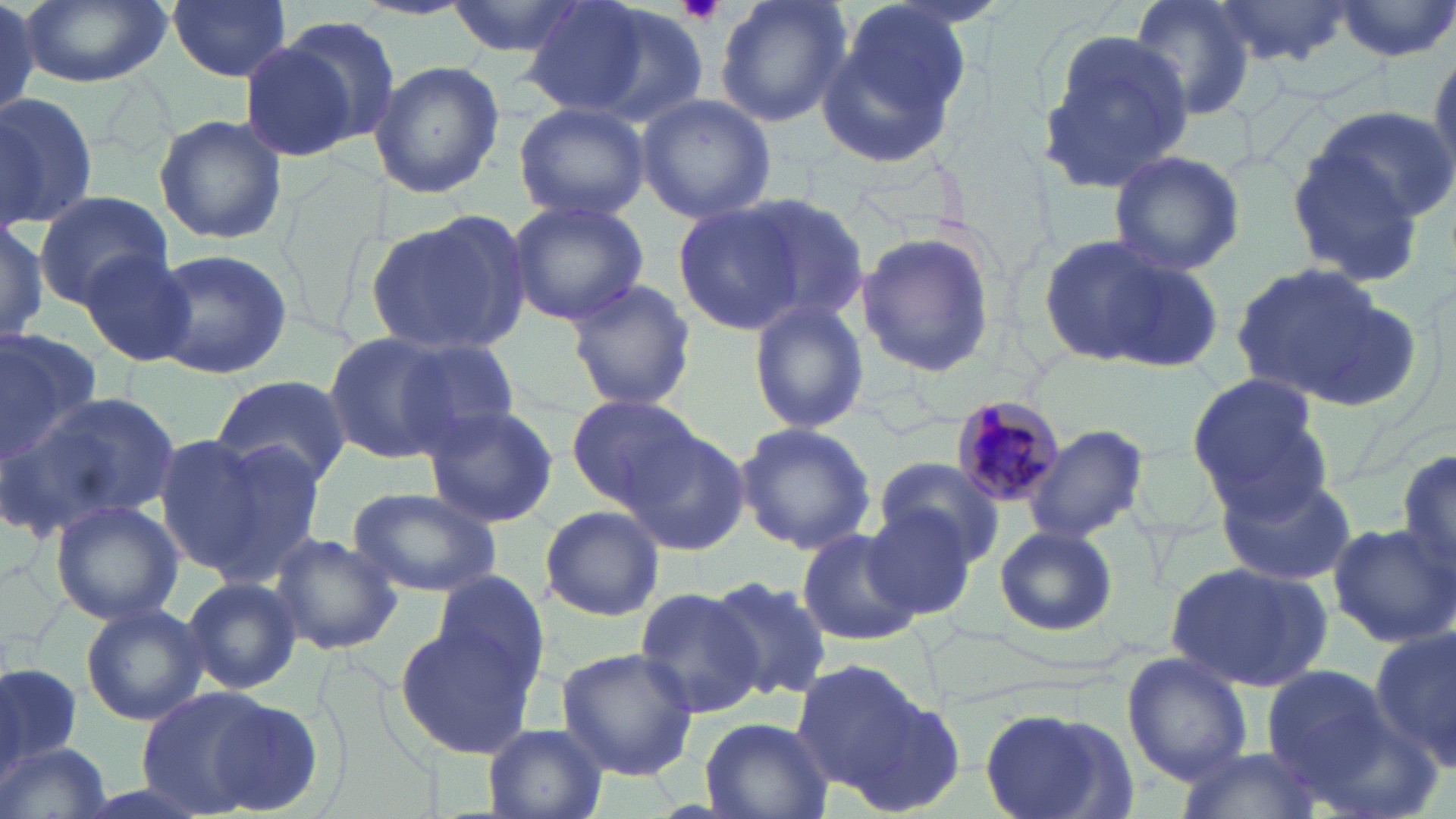

slide-level diagnosis = Plasmodium malariae
uninfected red blood cell locations = approximate bounding boxes as named x1/y1/x2/y2 corners in pixels: (x1=20, y1=0, x2=172, y2=88), (x1=165, y1=0, x2=293, y2=82), (x1=442, y1=0, x2=592, y2=59), (x1=523, y1=0, x2=684, y2=122), (x1=715, y1=0, x2=851, y2=128), (x1=1128, y1=0, x2=1258, y2=124), (x1=1216, y1=0, x2=1356, y2=69), (x1=0, y1=1, x2=50, y2=121), (x1=1333, y1=1, x2=1456, y2=61), (x1=817, y1=7, x2=971, y2=170), (x1=275, y1=15, x2=403, y2=148), (x1=1037, y1=29, x2=1197, y2=197), (x1=240, y1=42, x2=363, y2=161), (x1=1427, y1=43, x2=1456, y2=189), (x1=369, y1=60, x2=504, y2=197), (x1=0, y1=89, x2=101, y2=227), (x1=635, y1=93, x2=776, y2=224), (x1=514, y1=102, x2=651, y2=223), (x1=1307, y1=104, x2=1453, y2=224), (x1=154, y1=114, x2=289, y2=247), (x1=1284, y1=145, x2=1431, y2=288), (x1=1104, y1=150, x2=1246, y2=278), (x1=33, y1=189, x2=172, y2=307), (x1=739, y1=194, x2=869, y2=324), (x1=506, y1=198, x2=649, y2=326), (x1=674, y1=203, x2=807, y2=333), (x1=365, y1=210, x2=530, y2=356), (x1=0, y1=211, x2=52, y2=348), (x1=855, y1=229, x2=995, y2=380), (x1=1034, y1=231, x2=1195, y2=366), (x1=147, y1=246, x2=293, y2=381), (x1=75, y1=249, x2=197, y2=367), (x1=1098, y1=253, x2=1225, y2=376), (x1=1225, y1=260, x2=1416, y2=408), (x1=561, y1=278, x2=697, y2=413), (x1=747, y1=299, x2=871, y2=434), (x1=0, y1=326, x2=103, y2=460), (x1=320, y1=333, x2=467, y2=465), (x1=385, y1=333, x2=523, y2=453), (x1=1186, y1=371, x2=1329, y2=511), (x1=210, y1=373, x2=351, y2=491), (x1=13, y1=389, x2=182, y2=537), (x1=564, y1=394, x2=705, y2=506), (x1=420, y1=403, x2=559, y2=529), (x1=735, y1=421, x2=878, y2=554), (x1=620, y1=425, x2=750, y2=556), (x1=1023, y1=425, x2=1147, y2=545), (x1=152, y1=436, x2=273, y2=575), (x1=197, y1=436, x2=333, y2=581), (x1=1396, y1=447, x2=1456, y2=580), (x1=874, y1=457, x2=1004, y2=566), (x1=1212, y1=470, x2=1356, y2=586), (x1=346, y1=484, x2=504, y2=597), (x1=49, y1=499, x2=186, y2=626), (x1=863, y1=503, x2=981, y2=622), (x1=539, y1=504, x2=665, y2=621), (x1=1326, y1=520, x2=1454, y2=647), (x1=994, y1=524, x2=1118, y2=638), (x1=796, y1=527, x2=921, y2=647), (x1=267, y1=531, x2=404, y2=655), (x1=1165, y1=560, x2=1333, y2=689), (x1=429, y1=568, x2=552, y2=695), (x1=182, y1=575, x2=302, y2=694), (x1=710, y1=575, x2=834, y2=701), (x1=632, y1=586, x2=767, y2=719), (x1=77, y1=603, x2=206, y2=723), (x1=396, y1=624, x2=537, y2=757), (x1=1370, y1=625, x2=1456, y2=766), (x1=554, y1=647, x2=699, y2=780), (x1=1122, y1=652, x2=1253, y2=786), (x1=790, y1=658, x2=930, y2=800), (x1=0, y1=662, x2=85, y2=781), (x1=1261, y1=663, x2=1395, y2=790), (x1=135, y1=687, x2=289, y2=816), (x1=846, y1=694, x2=966, y2=818), (x1=977, y1=705, x2=1136, y2=819), (x1=696, y1=717, x2=833, y2=819), (x1=480, y1=725, x2=609, y2=819), (x1=0, y1=740, x2=115, y2=819), (x1=1176, y1=747, x2=1321, y2=819)
modality = optical microscopy
stain = May-Grünwald-Giemsa
platelet locations = approximate bounding boxes as named x1/y1/x2/y2 corners in pixels: (x1=678, y1=2, x2=727, y2=24)
Plasmodium malariae-infected red blood cell locations = approximate bounding boxes as named x1/y1/x2/y2 corners in pixels: (x1=949, y1=395, x2=1069, y2=511)
image size = 1456×819 pixels
field of view = one of a larger specimen
magnification = 1000x
preparation = thin blood film